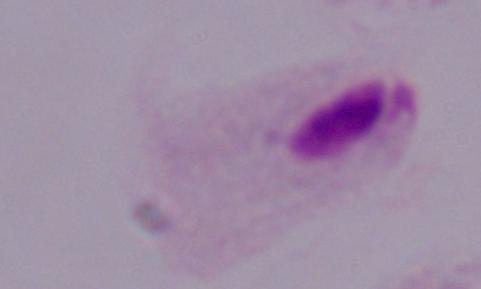
Captured at 1000x magnification. A trichomonad is shown. Photomicrograph.